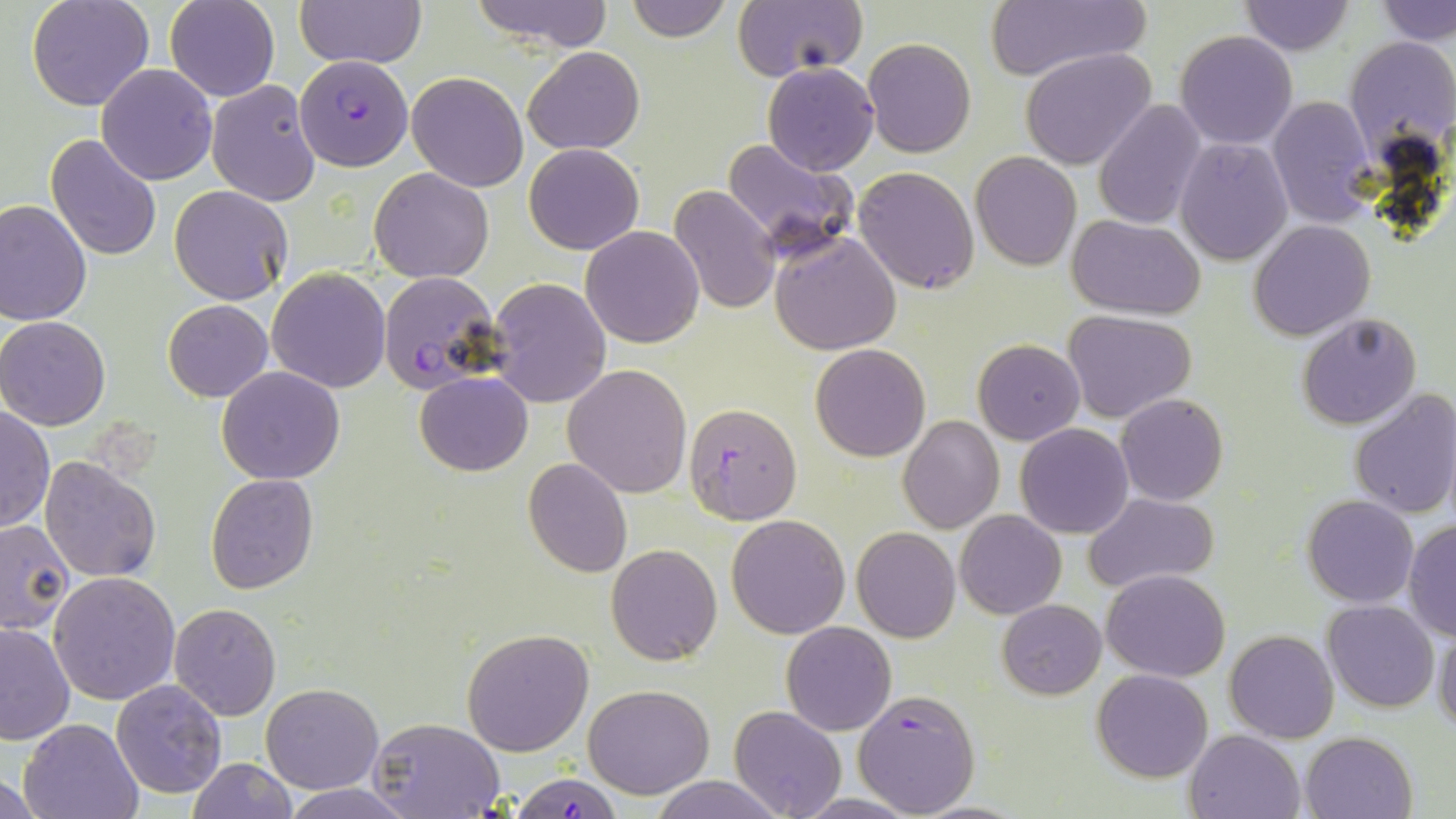
slide-level diagnosis = Plasmodium falciparum
uninfected red blood cell locations = approximate bounding boxes as (x1, y1, x2, y2) in pixels: (27, 0, 156, 111), (165, 0, 279, 102), (293, 0, 426, 68), (470, 0, 615, 51), (622, 0, 733, 42), (731, 1, 866, 83), (1237, 1, 1355, 55), (1378, 1, 1456, 45), (986, 3, 1145, 81), (1174, 30, 1297, 150), (1344, 36, 1456, 160), (863, 37, 976, 157), (523, 46, 644, 156), (1020, 48, 1157, 170), (762, 62, 878, 175), (95, 64, 218, 185), (407, 72, 529, 192), (206, 79, 322, 207), (1267, 95, 1375, 227), (1094, 100, 1208, 230), (45, 133, 163, 261), (1174, 137, 1292, 265), (720, 139, 858, 260), (523, 143, 645, 255), (970, 152, 1082, 272), (853, 166, 980, 296), (369, 167, 493, 282), (169, 185, 292, 304), (668, 185, 780, 315), (0, 197, 92, 325), (1066, 216, 1208, 320), (1249, 220, 1376, 340), (580, 226, 705, 347), (770, 229, 902, 355), (266, 267, 393, 392), (487, 277, 612, 408), (163, 299, 273, 402), (1062, 309, 1199, 425), (1296, 313, 1422, 429), (0, 316, 110, 430), (973, 338, 1085, 444), (810, 344, 929, 461), (562, 364, 693, 499), (216, 366, 346, 483), (414, 372, 534, 476), (1349, 388, 1456, 521), (1116, 394, 1229, 506), (0, 408, 54, 534), (898, 414, 1003, 534), (1014, 423, 1133, 539), (40, 455, 161, 584), (523, 457, 632, 577), (206, 473, 319, 593), (1086, 492, 1219, 593), (1301, 495, 1418, 607), (955, 510, 1065, 619), (726, 514, 851, 639), (1403, 519, 1456, 641), (0, 520, 74, 634), (851, 527, 960, 643), (606, 544, 722, 665), (1101, 568, 1230, 682), (49, 571, 181, 704), (998, 600, 1105, 699), (1323, 601, 1439, 713), (170, 602, 282, 720), (0, 621, 75, 745), (782, 622, 896, 736), (1433, 623, 1456, 733), (462, 628, 595, 757), (1225, 630, 1338, 743), (1092, 668, 1213, 782), (111, 680, 226, 799), (261, 683, 383, 794), (584, 684, 715, 799), (728, 705, 846, 818), (19, 716, 145, 819), (367, 716, 506, 819), (1184, 729, 1307, 819), (1300, 731, 1418, 819), (186, 759, 296, 818), (0, 769, 45, 819), (648, 775, 784, 818), (278, 784, 419, 819)
stain = May-Grünwald-Giemsa
Plasmodium falciparum-infected red blood cell locations = approximate bounding boxes as (x1, y1, x2, y2) in pixels: (293, 58, 412, 164), (378, 270, 501, 393), (681, 402, 802, 525), (854, 690, 981, 818), (508, 773, 626, 819)
field of view = single
modality = optical microscopy
magnification = 1000x
preparation = thin blood film
image size = 1456×819 pixels